State the blood parasite species.
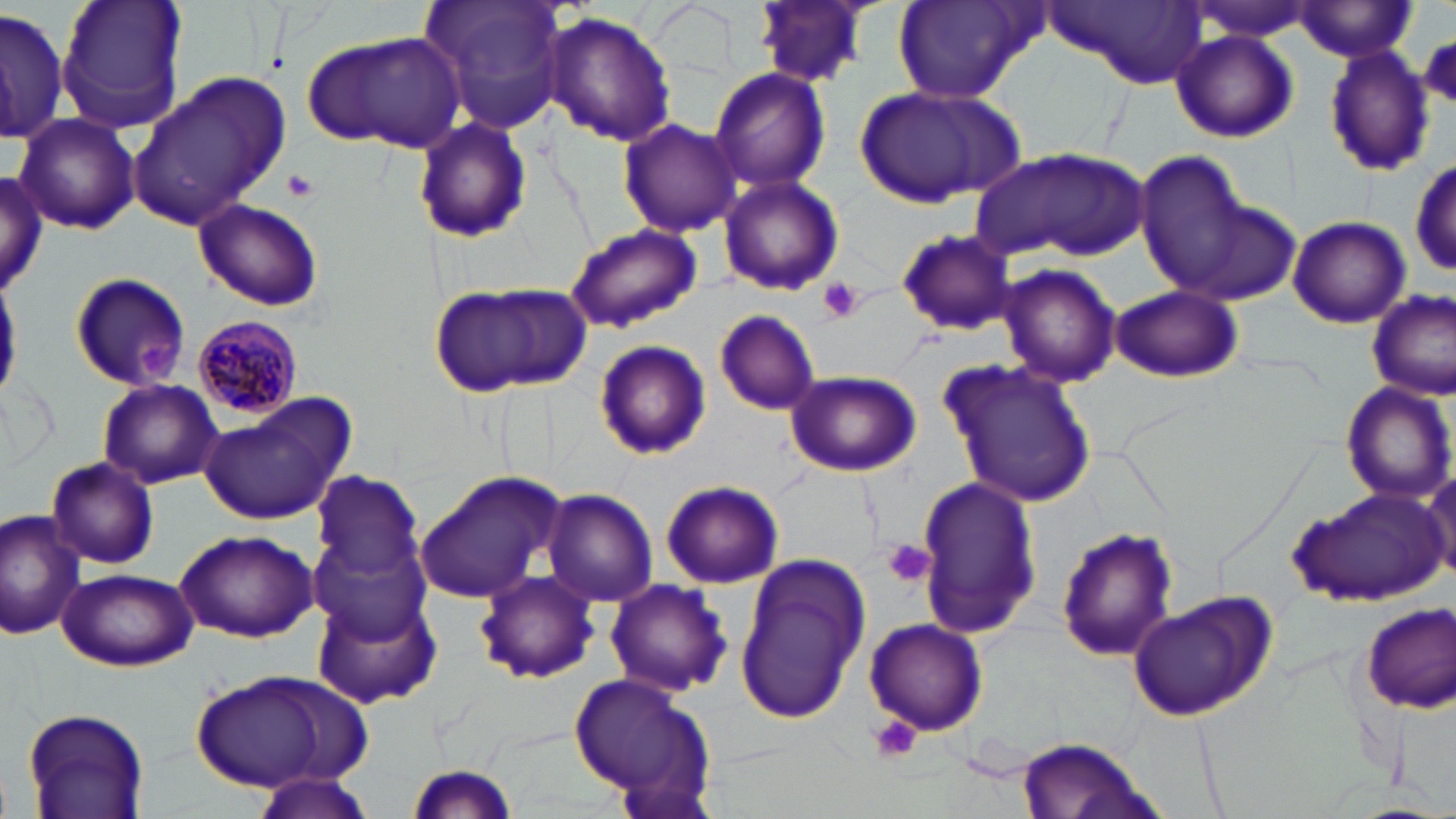
Plasmodium malariae.

modality = light microscopy
preparation = thin blood smear
stain = May-Grünwald-Giemsa
Plasmodium malariae-infected red blood cell locations = approximate bounding boxes as (x1, y1, x2, y2) in pixels: (191, 313, 302, 423)
field of view = single
image size = 1456×819 pixels
uninfected red blood cell locations = approximate bounding boxes as (x1, y1, x2, y2) in pixels: (53, 0, 190, 139), (418, 0, 571, 137), (753, 0, 874, 88), (1188, 0, 1320, 41), (893, 1, 1042, 104), (1039, 1, 1206, 88), (1291, 3, 1420, 59), (0, 8, 68, 143), (544, 12, 675, 147), (1170, 29, 1298, 143), (302, 32, 462, 151), (1322, 45, 1433, 178), (708, 65, 833, 192), (128, 72, 296, 229), (852, 83, 1026, 209), (12, 114, 141, 236), (411, 116, 532, 244), (617, 117, 742, 237), (972, 147, 1144, 264), (1135, 148, 1248, 292), (1411, 157, 1455, 277), (0, 173, 50, 301), (718, 174, 846, 297), (194, 198, 324, 312), (1173, 199, 1302, 308), (1287, 215, 1411, 328), (563, 223, 702, 334), (894, 228, 1018, 337), (997, 263, 1122, 389), (67, 271, 193, 391), (427, 281, 589, 399), (1109, 285, 1244, 383), (1366, 288, 1455, 401), (714, 309, 820, 415), (592, 338, 712, 460), (939, 356, 1099, 510), (784, 369, 922, 477), (97, 378, 223, 490), (1341, 383, 1453, 501), (200, 395, 355, 526), (46, 455, 160, 569), (412, 470, 569, 605), (1425, 471, 1456, 586), (311, 474, 423, 581), (916, 475, 1038, 639), (660, 479, 785, 589), (1285, 484, 1449, 604), (542, 488, 657, 608), (0, 509, 86, 640), (309, 518, 436, 644), (1058, 527, 1178, 662), (173, 530, 316, 641), (734, 552, 870, 725), (55, 569, 196, 670), (472, 571, 599, 686), (604, 578, 733, 698), (314, 589, 440, 709), (1126, 590, 1280, 723), (1359, 603, 1456, 711), (863, 617, 988, 736), (187, 671, 365, 793), (570, 671, 714, 805), (21, 705, 149, 817), (1015, 738, 1159, 819), (403, 760, 521, 818), (249, 772, 376, 819)
magnification = 1000x
platelet locations = approximate bounding boxes as (x1, y1, x2, y2) in pixels: (281, 170, 317, 201), (820, 278, 867, 323), (885, 538, 933, 587), (868, 717, 924, 766)